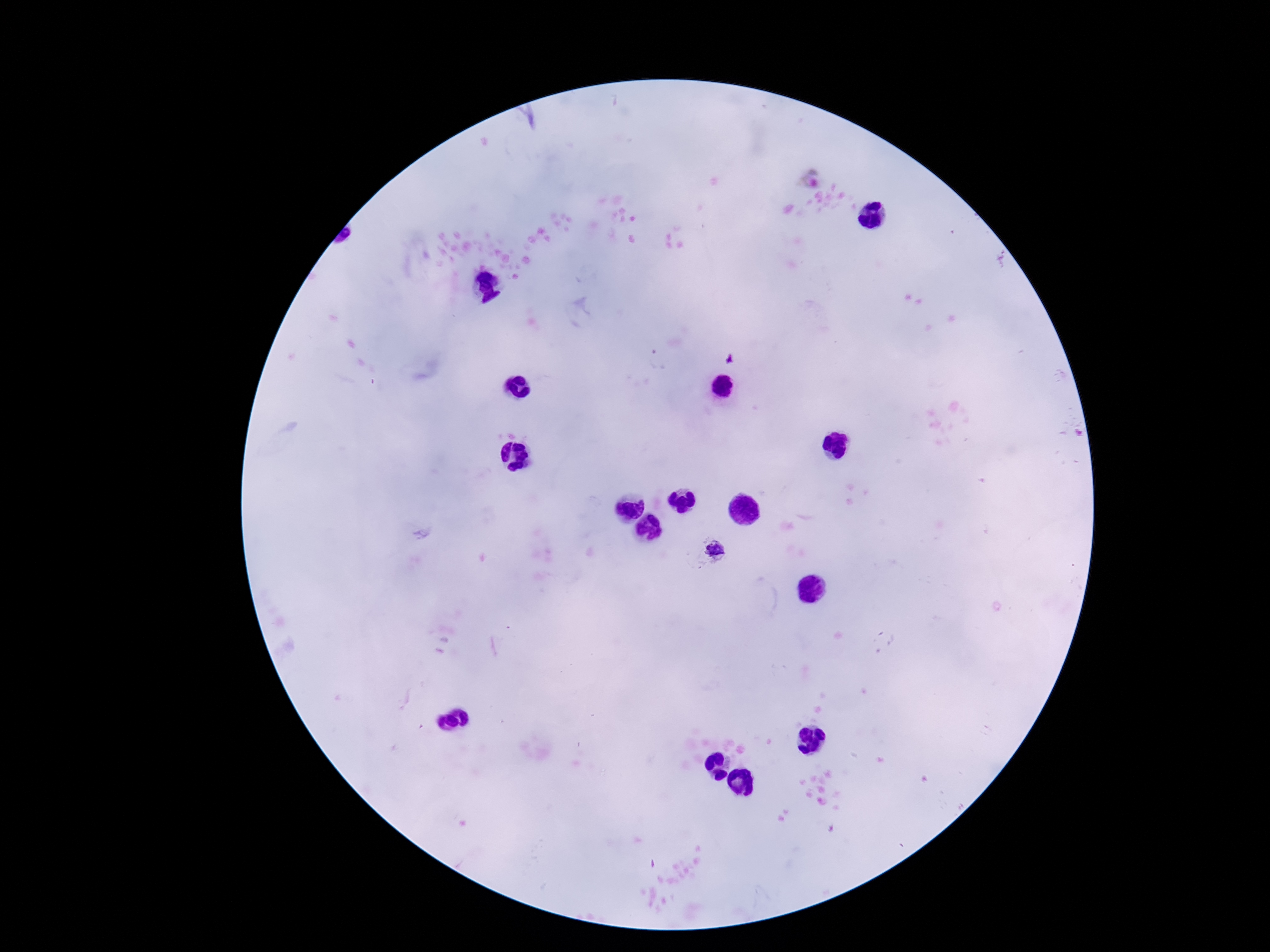

Approximate centers as {x, y} in pixels. Plasmodium parasite locations: {715, 548}. Giemsa stain. Image is 1270×952 pixels. Single field of view. Patient malaria status: infected. 100x magnification. Photographed through the microscope eyepiece with a smartphone camera. Thick blood smear.